Give the extent of all Trypanosoma brucei.
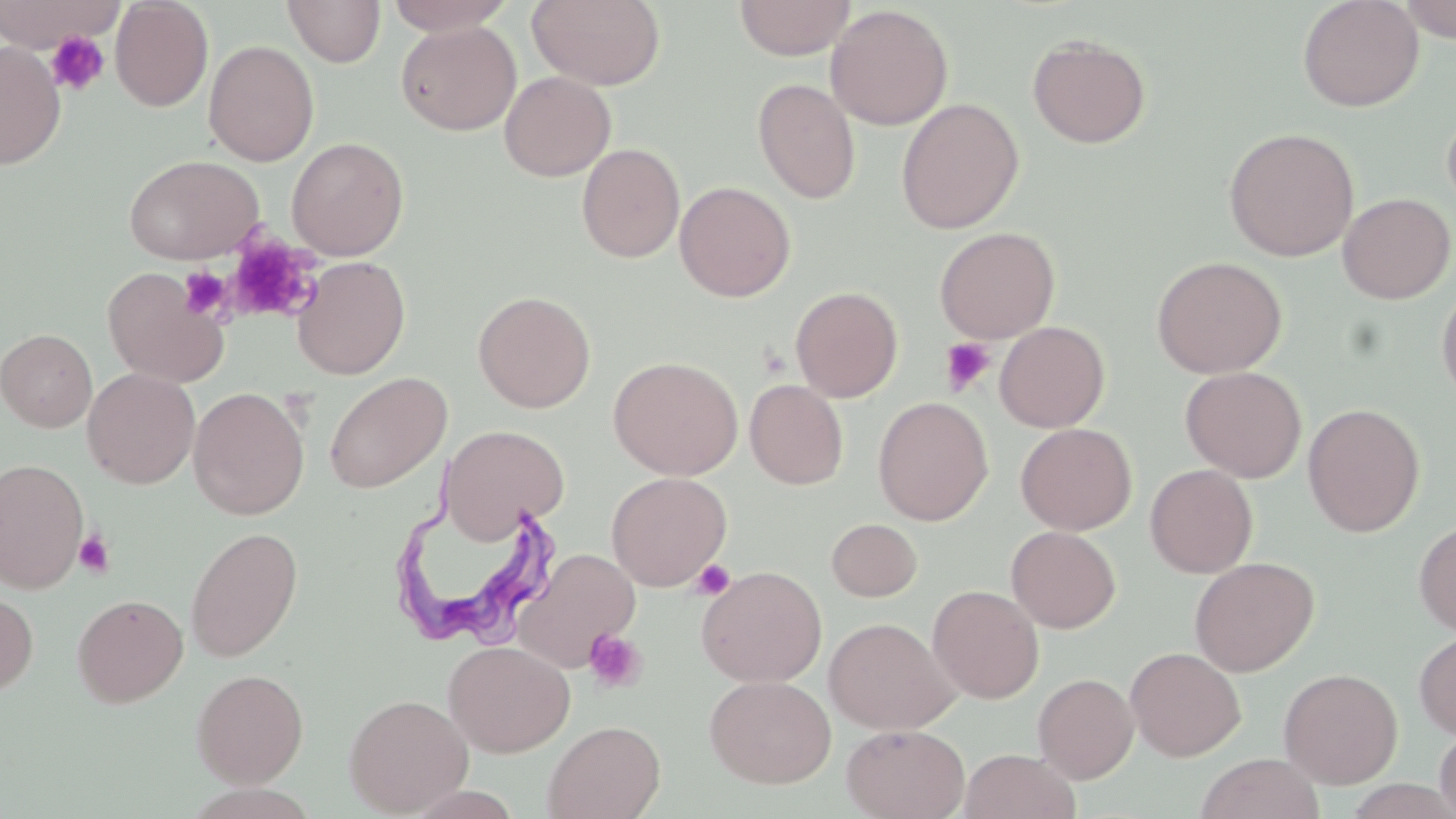
Approximate bounding boxes as [x1, y1, x2, y2] in pixels.
Trypanosoma brucei: [390, 502, 559, 653].

Summary:
  - Uninfected red blood cell locations: [0, 0, 125, 50], [110, 0, 214, 112], [384, 0, 517, 36], [527, 0, 666, 91], [734, 0, 856, 60], [1297, 0, 1424, 112], [1396, 0, 1456, 42], [282, 1, 386, 67], [826, 4, 953, 130], [396, 20, 521, 136], [1027, 34, 1151, 148], [203, 40, 319, 166], [0, 41, 66, 169], [499, 70, 616, 182], [752, 77, 861, 204], [895, 98, 1024, 234], [1442, 107, 1456, 218], [1223, 127, 1360, 261], [286, 136, 409, 260], [576, 142, 685, 263], [123, 153, 265, 265], [674, 180, 796, 302], [1337, 192, 1455, 304], [934, 226, 1060, 342], [292, 256, 410, 380], [1151, 256, 1288, 379], [102, 267, 228, 387], [1436, 281, 1456, 408], [790, 285, 903, 402], [473, 290, 596, 413], [994, 321, 1110, 433], [0, 328, 97, 431], [607, 355, 743, 480], [1180, 366, 1307, 482], [82, 368, 200, 488], [323, 372, 452, 494], [745, 379, 849, 489], [189, 387, 309, 520], [873, 396, 993, 526], [1302, 403, 1425, 536], [1015, 422, 1137, 535], [440, 424, 570, 544], [0, 458, 89, 593], [1144, 464, 1258, 578], [606, 471, 731, 590], [826, 518, 923, 601], [1414, 519, 1456, 636], [1006, 525, 1121, 633], [186, 527, 303, 662], [514, 548, 641, 671], [1189, 556, 1319, 677], [696, 565, 827, 687], [928, 584, 1044, 703], [0, 586, 39, 699], [72, 593, 189, 708], [824, 617, 958, 734], [1414, 630, 1456, 740], [443, 640, 575, 756], [1125, 646, 1246, 761], [1279, 668, 1403, 788], [191, 669, 309, 787], [1033, 673, 1139, 783], [704, 674, 836, 788], [344, 693, 474, 816], [543, 720, 666, 819], [840, 723, 970, 819], [1433, 726, 1456, 819], [958, 749, 1081, 819], [1195, 753, 1326, 819]
  - Platelet locations: [45, 30, 109, 96], [224, 235, 319, 324], [179, 266, 233, 321], [940, 337, 996, 396], [73, 529, 116, 579], [691, 559, 735, 600], [583, 628, 647, 694]
  - Slide-level diagnosis: Trypanosoma brucei
  - Modality: optical microscopy
  - Stain: May-Grünwald-Giemsa
  - Image size: 1456×819 pixels
  - Preparation: thin blood smear
  - Magnification: 1000x
  - Field of view: one of a larger specimen